State which parasite is depicted.
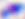
This is Toxoplasma gondii.

Photomicrograph. 400x magnification.